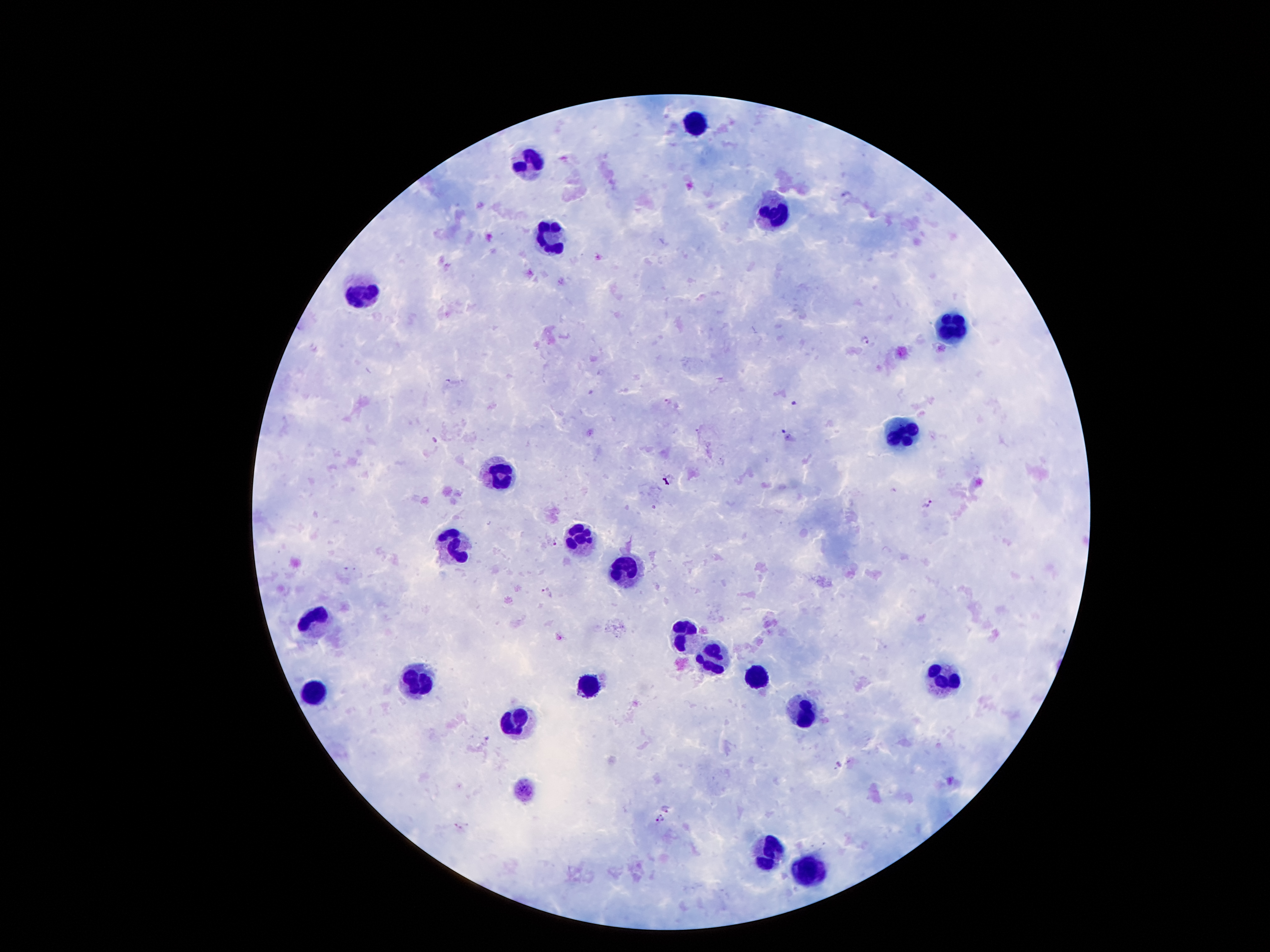
Approximate centers as {x, y} in pixels.
Summary:
  - Malaria parasite locations: {846, 195}, {866, 340}, {795, 403}, {785, 431}, {435, 440}, {669, 481}, {927, 502}, {553, 540}, {545, 592}, {560, 637}, {489, 737}, {838, 764}, {667, 808}, {658, 820}
  - Leukocyte locations: {691, 122}, {529, 152}, {773, 214}, {551, 237}, {359, 294}, {955, 328}, {903, 432}, {497, 471}, {581, 539}, {451, 546}, {627, 570}, {313, 616}, {685, 634}, {713, 658}, {949, 675}, {759, 678}, {419, 679}, {581, 688}, {311, 694}, {803, 710}, {515, 718}, {769, 850}, {811, 866}
  - Magnification: 100x
  - Stain: Giemsa
  - Field of view: single
  - Image size: 1270×952 pixels
  - Capture: smartphone through the microscope eyepiece
  - Preparation: thick blood smear
  - Patient malaria status: infected with Plasmodium falciparum